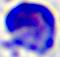

Summary:
  - Magnification: 400x
  - Modality: micrograph
  - Identification: leukocyte